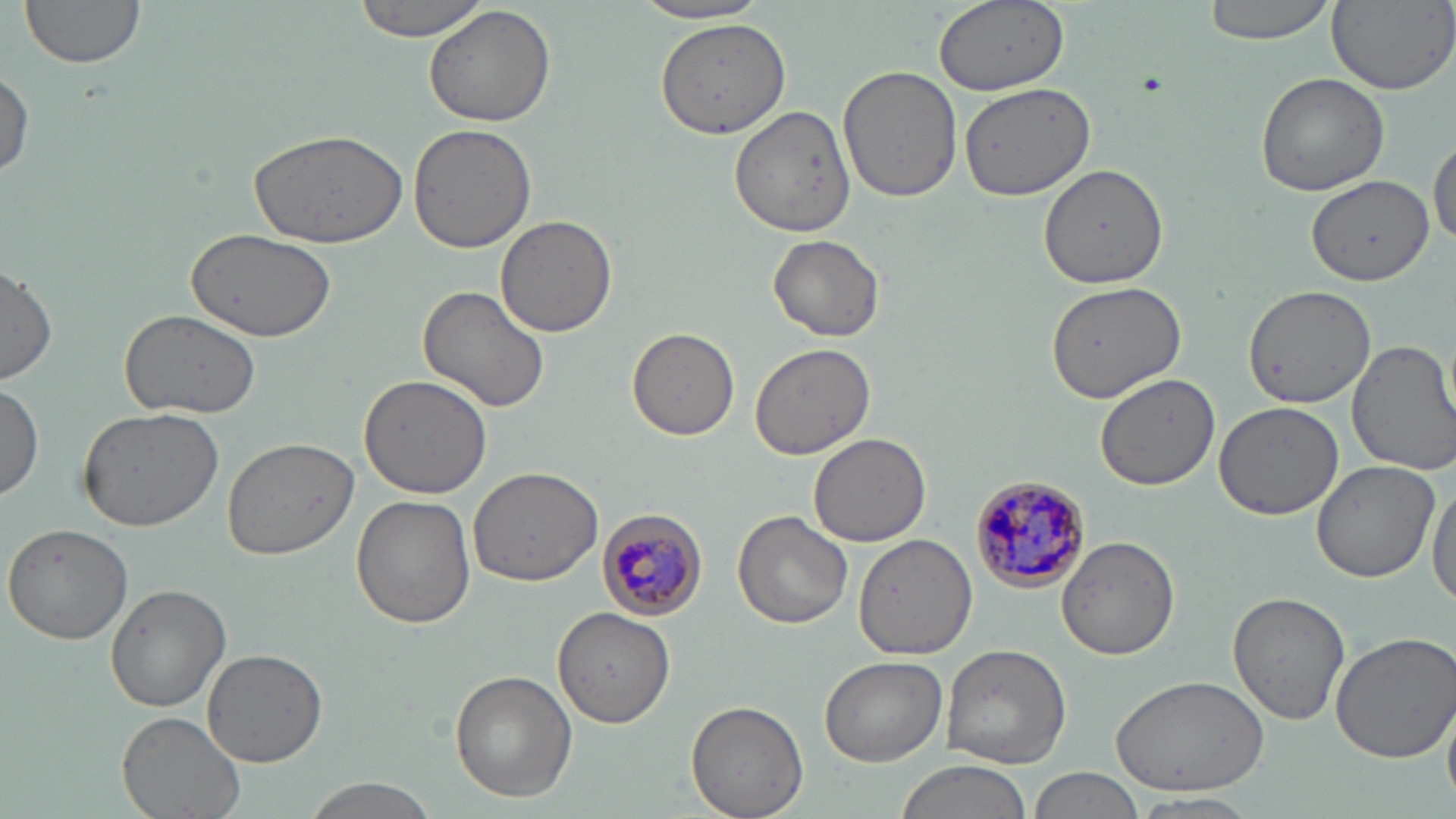 Approximate bounding boxes as (x1,y1)-(x2,y2) corner pairs in pixels. Uninfected red blood cell locations: (19,0)-(150,71), (352,0)-(491,41), (933,0)-(1070,93), (1201,0)-(1338,43), (1327,0)-(1456,98), (632,1)-(775,27), (424,5)-(556,128), (653,16)-(792,139), (838,62)-(964,201), (0,67)-(34,184), (1254,72)-(1389,197), (957,83)-(1096,202), (731,103)-(857,237), (406,124)-(538,254), (249,128)-(409,247), (1429,134)-(1455,249), (1038,162)-(1170,288), (1308,175)-(1431,285), (495,214)-(618,338), (186,228)-(339,347), (769,235)-(885,343), (1,263)-(58,384), (1044,282)-(1187,402), (417,283)-(552,414), (1241,283)-(1376,409), (120,307)-(261,419), (628,326)-(741,440), (1347,339)-(1456,474), (750,343)-(875,460), (358,373)-(496,500), (1096,374)-(1219,491), (0,379)-(45,501), (1212,400)-(1344,520), (78,405)-(226,533), (808,432)-(931,547), (221,434)-(359,559), (1309,461)-(1441,584), (466,467)-(603,587), (1428,476)-(1456,613), (351,495)-(476,628), (732,509)-(853,630), (3,523)-(133,645), (854,535)-(978,659), (1058,536)-(1178,659), (105,584)-(230,711), (1226,590)-(1349,726), (553,606)-(675,725), (1327,629)-(1456,762), (940,644)-(1073,769), (202,650)-(327,766), (819,655)-(947,767), (450,670)-(576,803), (1108,673)-(1272,794), (1443,695)-(1456,801), (686,699)-(809,819), (117,711)-(244,819), (891,760)-(1030,819), (1027,766)-(1146,819), (297,776)-(439,818), (1131,793)-(1261,815). Plasmodium malariae-infected red blood cell locations: (967,477)-(1093,592), (596,510)-(710,623). Slide-level diagnosis: Plasmodium malariae. Light microscopy. 1000x magnification. Image is 1456×819 pixels. Thin blood smear. One field of a larger specimen. May-Grünwald-Giemsa stain.